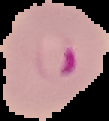
Summary:
  - Image type: segmented cell region on a black background
  - Preparation: thin blood smear
  - Image size: 109×121 pixels
  - Malaria status: parasitized